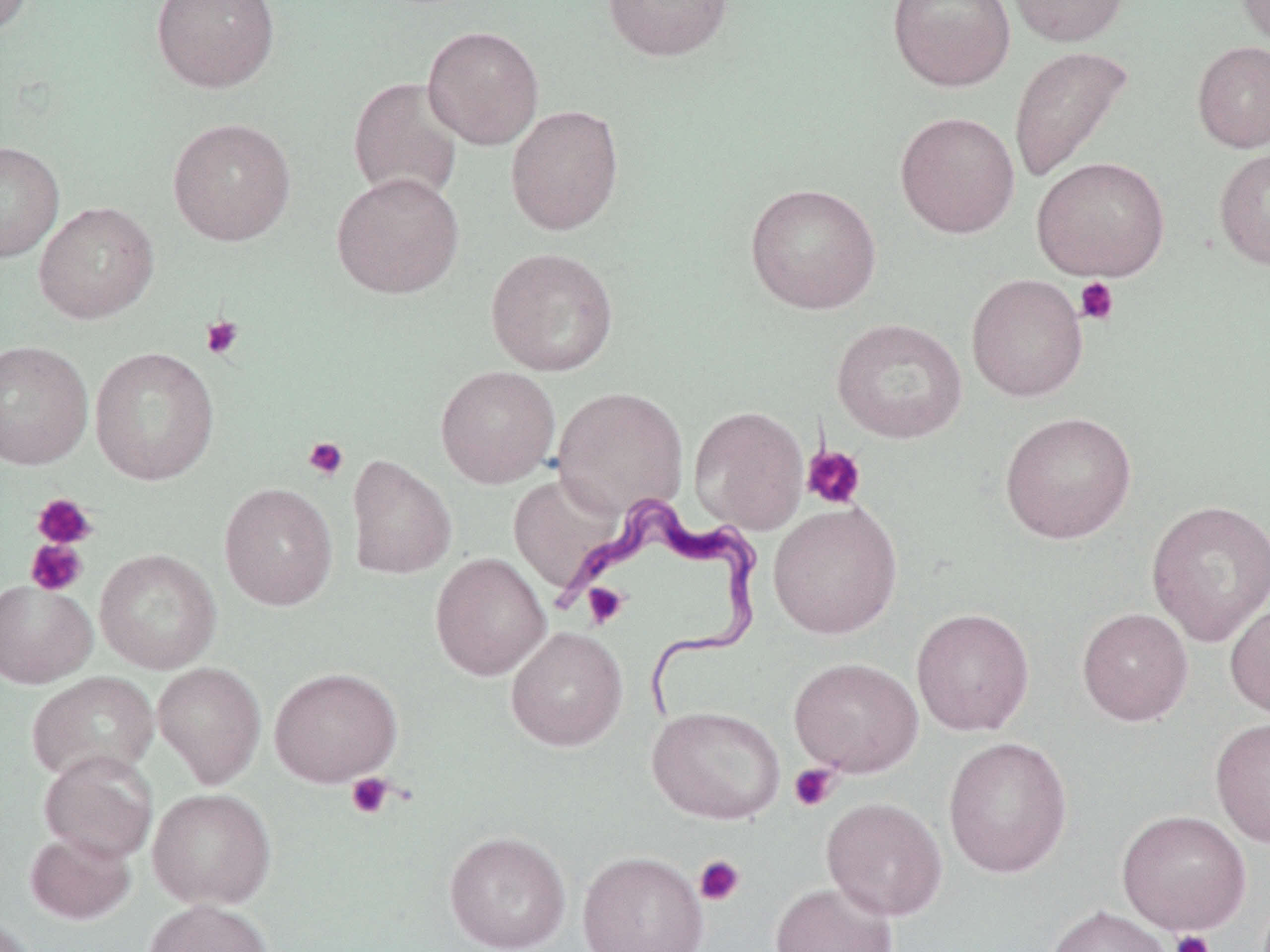
Summary:
  - Coordinate format: approximate bounding boxes as named x1/y1/x2/y2 corners in pixels
  - Trypanosoma brucei locations: (x1=569, y1=496, x2=765, y2=722)
  - Platelet locations: (x1=1075, y1=277, x2=1119, y2=325), (x1=200, y1=316, x2=244, y2=360), (x1=302, y1=436, x2=349, y2=481), (x1=802, y1=445, x2=867, y2=510), (x1=32, y1=493, x2=97, y2=550), (x1=25, y1=539, x2=88, y2=596), (x1=582, y1=583, x2=628, y2=629), (x1=788, y1=763, x2=840, y2=812), (x1=346, y1=772, x2=396, y2=819), (x1=694, y1=855, x2=746, y2=906), (x1=1169, y1=929, x2=1214, y2=952)
  - Uninfected red blood cell locations: (x1=0, y1=0, x2=35, y2=39), (x1=151, y1=0, x2=280, y2=93), (x1=603, y1=0, x2=734, y2=62), (x1=887, y1=0, x2=1015, y2=92), (x1=1004, y1=0, x2=1131, y2=47), (x1=1236, y1=0, x2=1270, y2=53), (x1=422, y1=25, x2=544, y2=150), (x1=1191, y1=40, x2=1270, y2=153), (x1=1008, y1=45, x2=1134, y2=184), (x1=347, y1=76, x2=464, y2=204), (x1=505, y1=104, x2=625, y2=235), (x1=895, y1=111, x2=1020, y2=238), (x1=167, y1=117, x2=296, y2=246), (x1=0, y1=141, x2=64, y2=262), (x1=1213, y1=146, x2=1270, y2=271), (x1=1031, y1=156, x2=1169, y2=281), (x1=331, y1=171, x2=465, y2=299), (x1=744, y1=182, x2=881, y2=315), (x1=34, y1=201, x2=159, y2=324), (x1=485, y1=247, x2=619, y2=377), (x1=966, y1=274, x2=1088, y2=402), (x1=831, y1=318, x2=967, y2=443), (x1=0, y1=340, x2=93, y2=470), (x1=89, y1=346, x2=220, y2=485), (x1=435, y1=365, x2=560, y2=488), (x1=553, y1=386, x2=688, y2=518), (x1=689, y1=405, x2=809, y2=534), (x1=999, y1=411, x2=1137, y2=544), (x1=346, y1=455, x2=457, y2=580), (x1=508, y1=472, x2=628, y2=598), (x1=218, y1=482, x2=339, y2=610), (x1=1147, y1=499, x2=1270, y2=647), (x1=768, y1=501, x2=902, y2=639), (x1=95, y1=549, x2=222, y2=673), (x1=430, y1=552, x2=551, y2=680), (x1=0, y1=580, x2=97, y2=688), (x1=1225, y1=599, x2=1270, y2=722), (x1=1077, y1=607, x2=1193, y2=726), (x1=911, y1=608, x2=1035, y2=736), (x1=505, y1=626, x2=627, y2=751), (x1=788, y1=657, x2=923, y2=776), (x1=152, y1=662, x2=266, y2=788), (x1=269, y1=666, x2=402, y2=786), (x1=26, y1=672, x2=160, y2=783), (x1=647, y1=705, x2=786, y2=825), (x1=1210, y1=716, x2=1270, y2=848), (x1=943, y1=736, x2=1073, y2=878), (x1=38, y1=749, x2=158, y2=864), (x1=147, y1=787, x2=277, y2=909), (x1=821, y1=796, x2=947, y2=921), (x1=1116, y1=810, x2=1251, y2=934), (x1=25, y1=830, x2=136, y2=924), (x1=444, y1=830, x2=571, y2=952), (x1=577, y1=849, x2=709, y2=952), (x1=770, y1=881, x2=898, y2=952), (x1=143, y1=898, x2=271, y2=952), (x1=1045, y1=905, x2=1173, y2=952), (x1=0, y1=915, x2=39, y2=951)
  - Slide-level diagnosis: Trypanosoma brucei
  - Modality: light microscopy
  - Stain: May-Grünwald-Giemsa
  - Field of view: single
  - Magnification: 1000x
  - Preparation: thin blood film
  - Image size: 1270×952 pixels